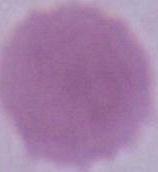

modality = photomicrograph
identification = red blood cell
magnification = 1000x